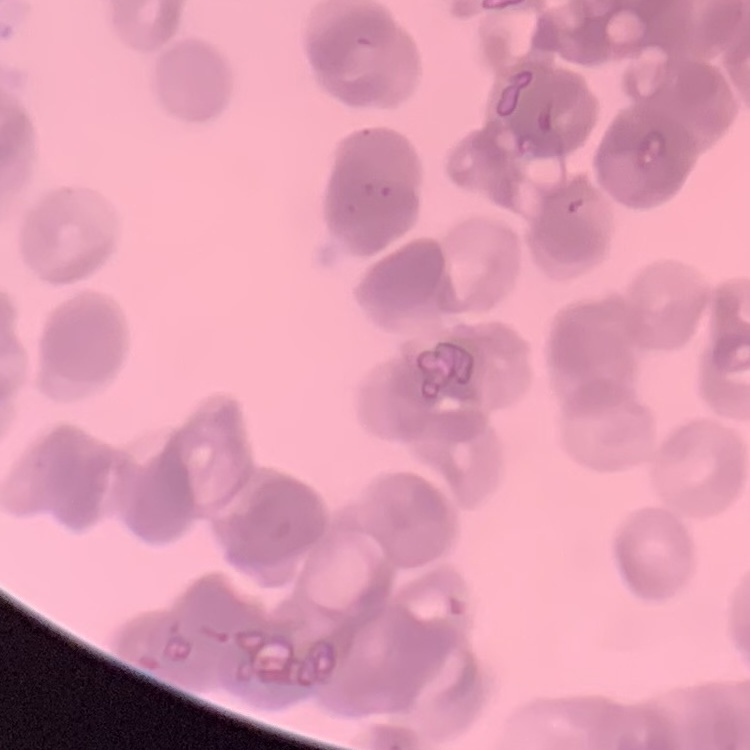 The red blood cells exhibit rouleaux formation. Thin blood film. One tile cut from a larger photomicrograph. Stained with either Field's or Giemsa.